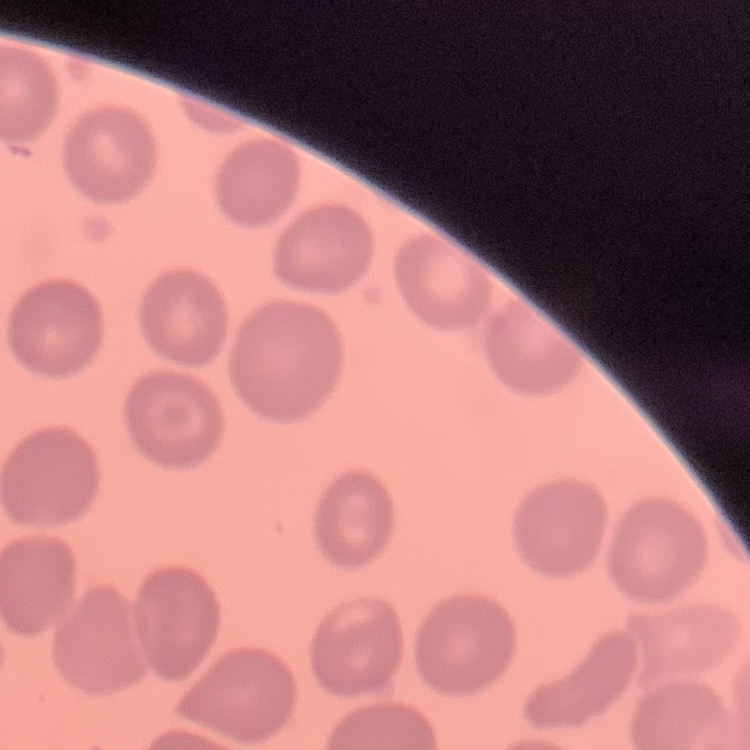

Summary:
  - Red blood cell morphology: no rouleaux formation
  - Image type: one tile cut from a larger photomicrograph
  - Stain: Field's or Giemsa
  - Preparation: thin blood film